Describe the morphology of the red blood cells.
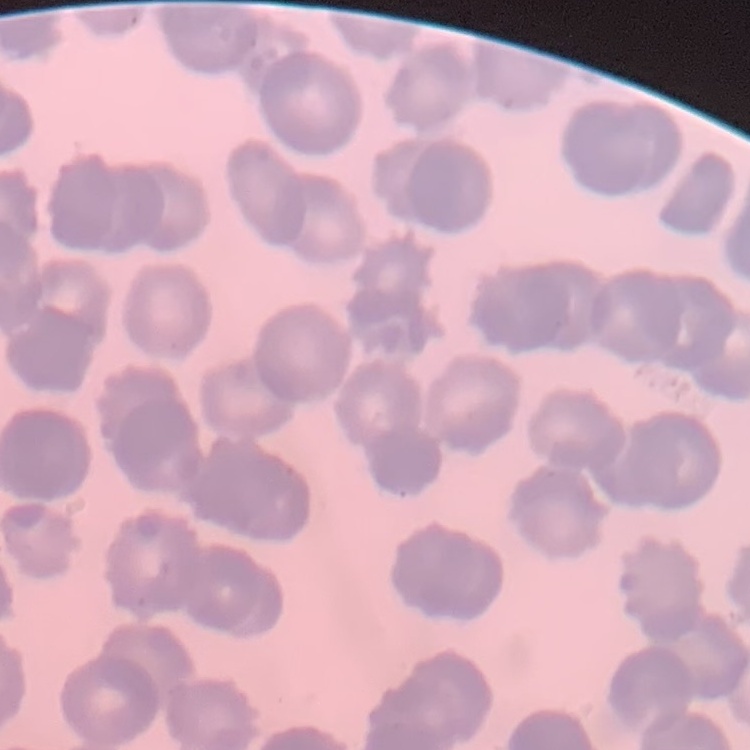

Rouleaux formation.

Field's or Giemsa stain. Thin blood film. One tile cut from a larger photomicrograph.